Assess this cell for malaria.
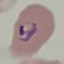
It is uninfected.

image type = cell patch, automatically extracted from a larger field of view and resized to 64 × 64 pixels
preparation = thin blood smear
stain = Giemsa
capture = smartphone through the microscope eyepiece